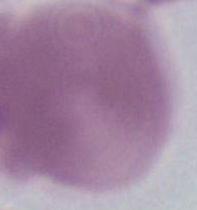 An erythrocyte is shown. Photomicrograph. 1000x magnification.